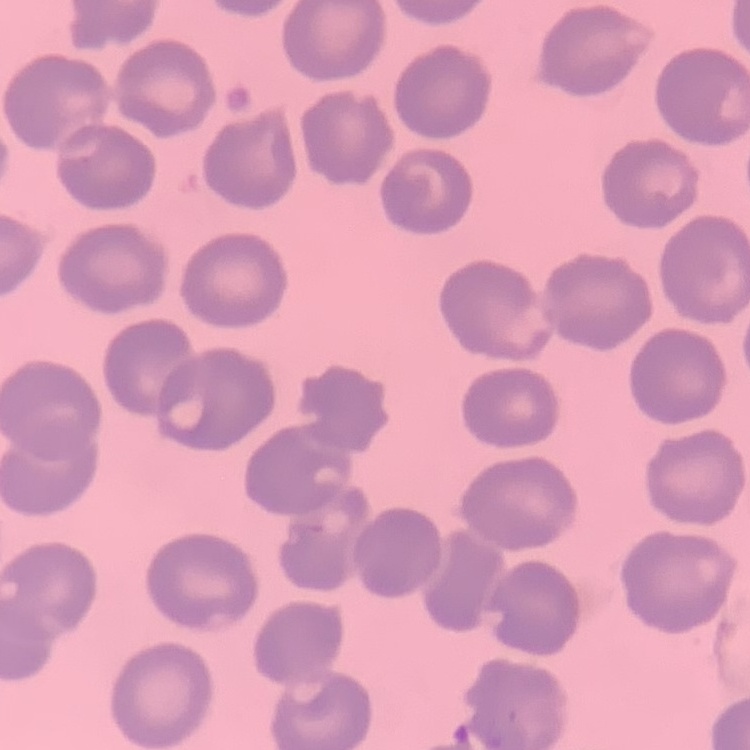

Summary:
  - Red blood cell morphology: no rouleaux formation
  - Stain: Field's or Giemsa
  - Image type: square crop of a larger photomicrograph
  - Preparation: thin blood smear